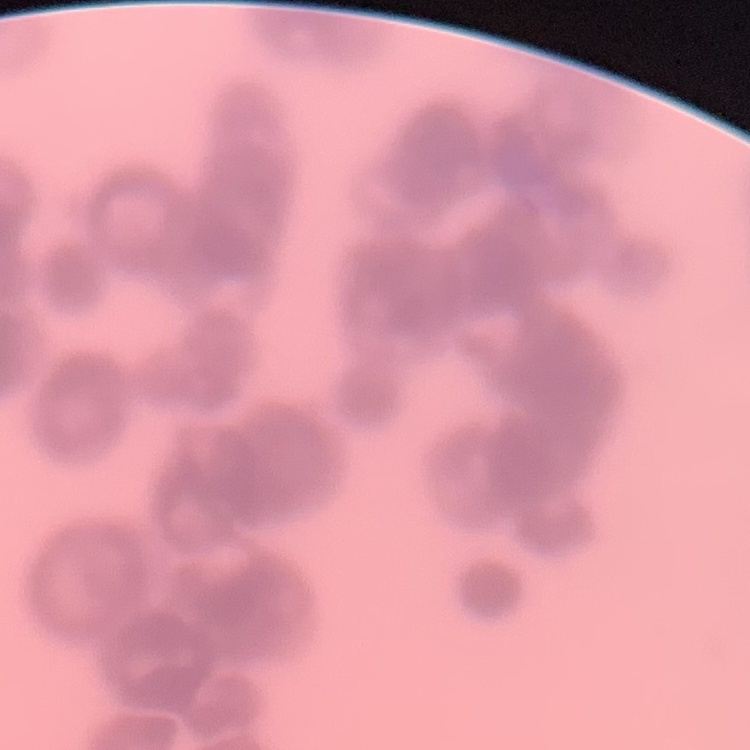
The red blood cells exhibit rouleaux formation. Thin peripheral smear. Square crop of a larger photomicrograph. Field's or Giemsa stain.